Give the position of each Plasmodium falciparum parasite with its life-cycle stage, each leukocyte, and any debris.
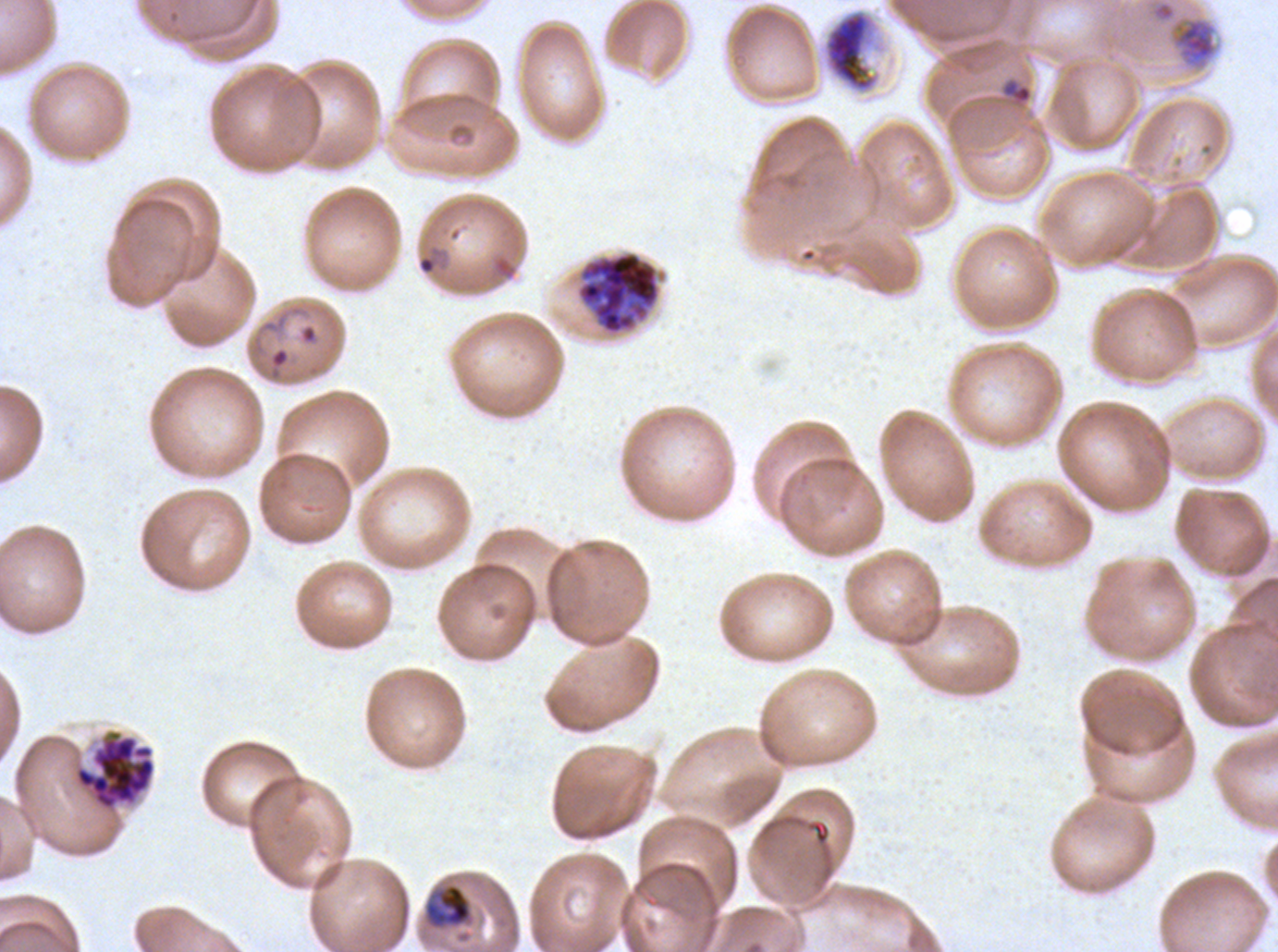
Approximate bounding boxes as {x1, y1, x2, y2} in pixels.
Rings: {1000, 78, 1033, 105}, {416, 244, 449, 276}, {268, 346, 290, 380}.
Mid trophozoites: {1167, 14, 1219, 71}, {423, 883, 473, 930}.
Late trophozoites: {817, 6, 889, 97}.
Late schizonts: {576, 250, 660, 336}.
Segmenters: {74, 735, 156, 811}.
No late-ring/early-trophozoite forms, early schizonts, gametocytes, leukocytes, or debris observed.

Thin blood smear. Image is 1278×952 pixels. Life-cycle stages observed: ring, mid trophozoite, late trophozoite, late schizont, segmenter. Giemsa-stained preparation. A sub-image separated from a larger composite. Plasmodium falciparum from a patient in The Gambia, cultured ex vivo for 24 to 48 hours.